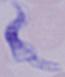

modality: photomicrograph
magnification: 1000x
identification: trypanosome